Identify the parasite.
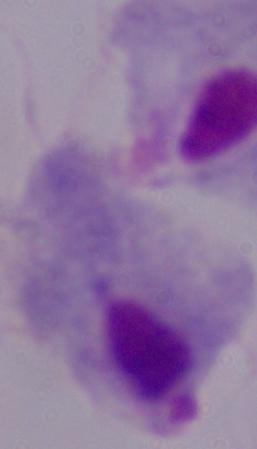

This is a trichomonad.

Summary:
  - Modality: micrograph
  - Magnification: 1000x